Locate every blood parasite and identify its species.
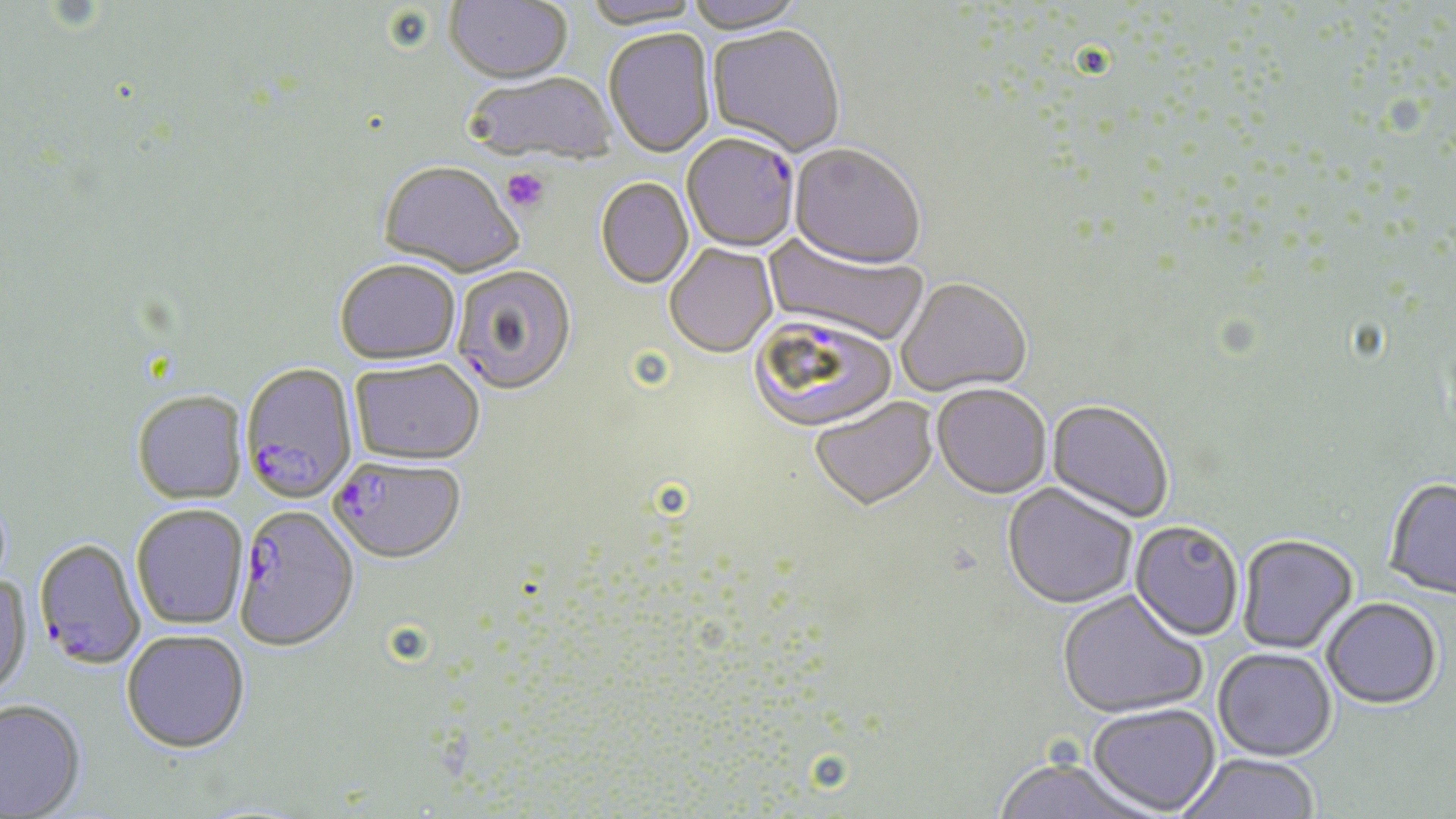

Approximate bounding boxes as named x1/y1/x2/y2 corners in pixels.
Plasmodium falciparum-infected red blood cells: (x1=682, y1=137, x2=798, y2=253), (x1=452, y1=266, x2=577, y2=396), (x1=748, y1=316, x2=899, y2=438), (x1=240, y1=365, x2=358, y2=506), (x1=330, y1=459, x2=465, y2=567), (x1=235, y1=507, x2=360, y2=654), (x1=34, y1=540, x2=146, y2=674).
No Plasmodium ovale, Plasmodium malariae, Plasmodium vivax, Babesia divergens, or Trypanosoma brucei observed.

Uninfected red blood cell locations: (x1=446, y1=0, x2=572, y2=87), (x1=583, y1=0, x2=704, y2=32), (x1=686, y1=0, x2=806, y2=36), (x1=707, y1=27, x2=845, y2=158), (x1=604, y1=30, x2=716, y2=160), (x1=465, y1=74, x2=617, y2=165), (x1=789, y1=146, x2=925, y2=272), (x1=378, y1=164, x2=521, y2=280), (x1=595, y1=179, x2=694, y2=291), (x1=762, y1=232, x2=927, y2=348), (x1=664, y1=246, x2=777, y2=361), (x1=334, y1=263, x2=461, y2=368), (x1=896, y1=280, x2=1032, y2=399), (x1=350, y1=361, x2=484, y2=469), (x1=932, y1=386, x2=1051, y2=501), (x1=132, y1=393, x2=248, y2=507), (x1=810, y1=400, x2=939, y2=513), (x1=1046, y1=401, x2=1173, y2=524), (x1=1384, y1=479, x2=1456, y2=601), (x1=1001, y1=485, x2=1137, y2=612), (x1=131, y1=507, x2=249, y2=632), (x1=1129, y1=522, x2=1243, y2=643), (x1=1237, y1=536, x2=1358, y2=655), (x1=0, y1=574, x2=33, y2=703), (x1=1057, y1=592, x2=1207, y2=721), (x1=1321, y1=598, x2=1443, y2=710), (x1=121, y1=632, x2=250, y2=756), (x1=1212, y1=649, x2=1337, y2=762), (x1=0, y1=700, x2=86, y2=818), (x1=1088, y1=705, x2=1221, y2=816), (x1=1176, y1=754, x2=1322, y2=818), (x1=991, y1=760, x2=1155, y2=819). Platelet locations: (x1=501, y1=169, x2=550, y2=213). Slide-level diagnosis: Plasmodium falciparum. Single field of view. Thin blood film. Image is 1456×819 pixels. 1000x magnification. Optical microscopy. May-Grünwald-Giemsa-stained preparation.